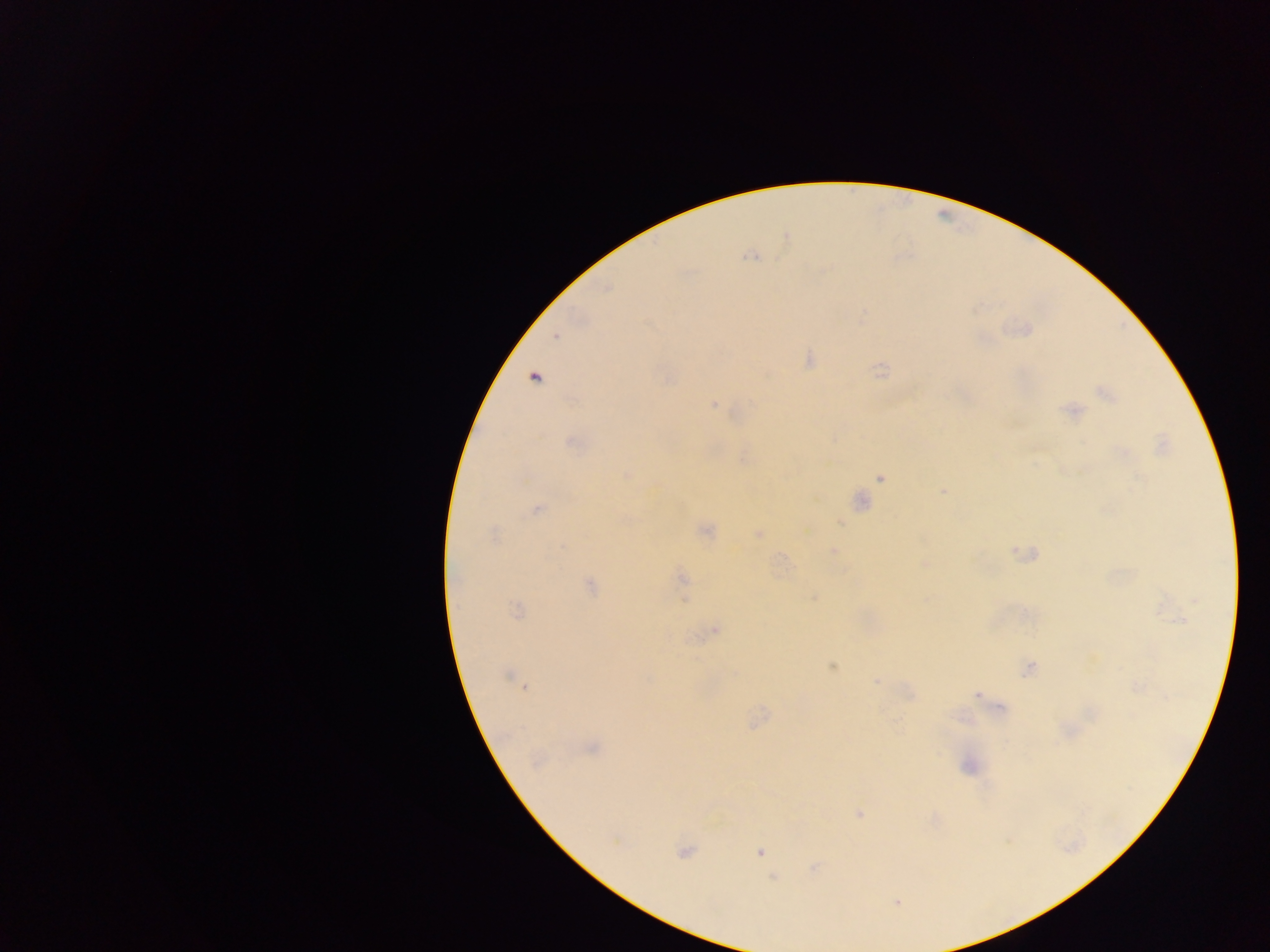

Approximate centers as (x, y) in pixels. Malaria parasite locations: (785, 238), (753, 256), (556, 335), (809, 360), (880, 370), (534, 377), (1106, 393), (714, 405), (1072, 411), (570, 441), (1162, 445), (626, 475), (881, 477), (942, 490), (859, 501), (536, 509), (838, 519), (706, 531), (493, 534), (758, 534), (833, 552), (1030, 554), (924, 564), (682, 578), (590, 585), (813, 597), (516, 610), (715, 629), (832, 667), (1029, 669), (509, 676), (877, 680), (518, 683), (524, 687), (977, 694), (757, 719), (591, 747), (968, 766), (859, 814), (684, 851), (758, 851), (814, 868), (773, 878), (896, 901). Sample from Ghana. Single field of view. Image is 1270×952 pixels. Mobile-phone photograph taken through the microscope. Thick blood film.